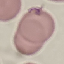

Summary:
  - Malaria status: uninfected
  - Preparation: thin blood smear
  - Capture: smartphone through the microscope eyepiece
  - Image type: cell patch, automatically extracted from a larger field of view and resized to 64 × 64 pixels
  - Stain: Giemsa